Identify the blood parasite species.
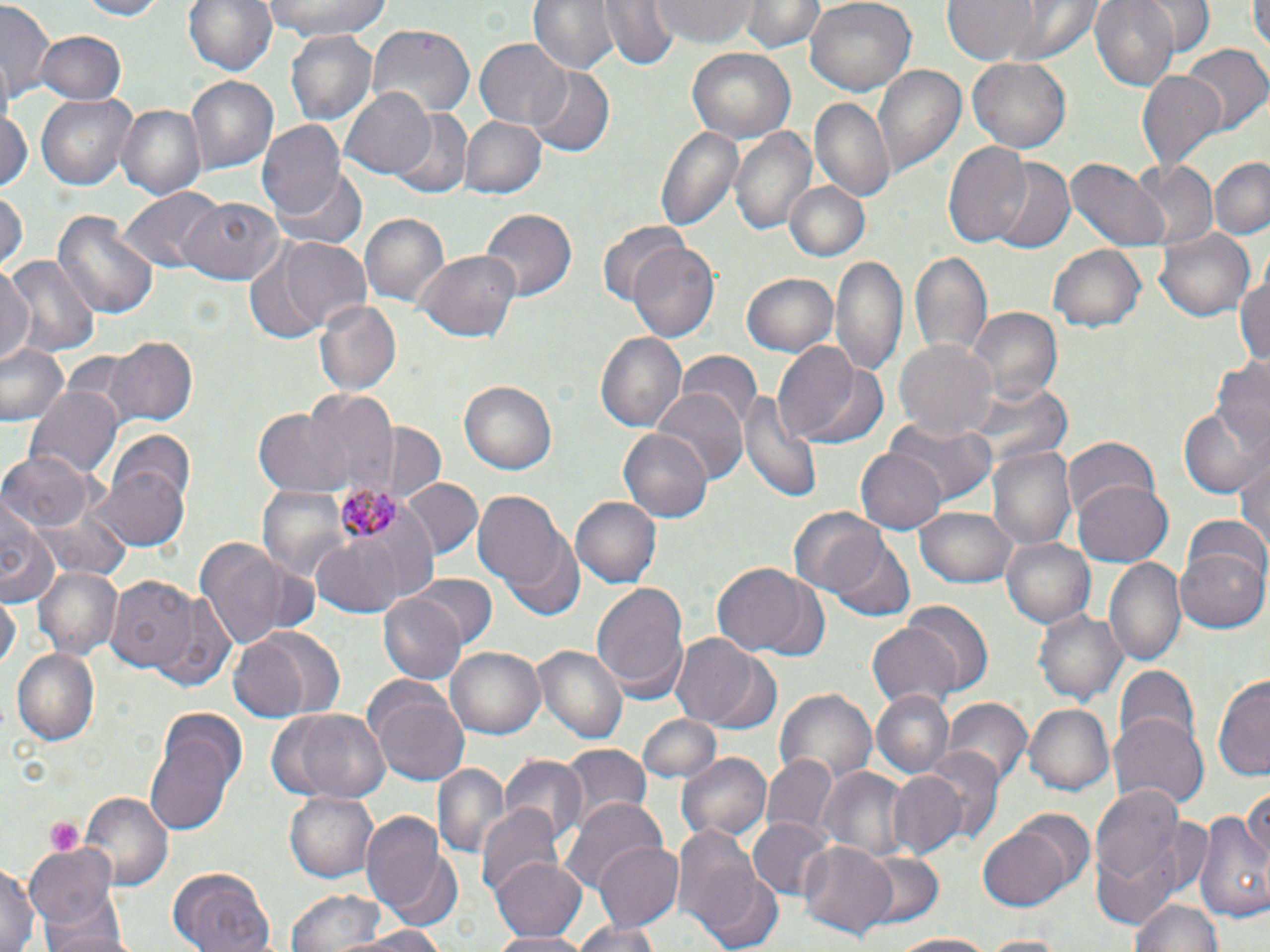

Plasmodium malariae.

stain = May-Grünwald-Giemsa
platelet locations = approximate bounding boxes as [x1, y1, x2, y2] in pixels: [45, 816, 84, 857]
preparation = thin blood smear
magnification = 1000x
uninfected red blood cell locations = approximate bounding boxes as [x1, y1, x2, y2] in pixels: [71, 0, 173, 20], [184, 0, 276, 80], [256, 0, 396, 42], [530, 0, 620, 76], [599, 0, 679, 71], [650, 0, 756, 46], [745, 0, 822, 55], [804, 0, 916, 96], [943, 0, 1041, 68], [1090, 0, 1180, 90], [1144, 0, 1214, 56], [1252, 0, 1270, 57], [0, 3, 56, 107], [366, 26, 475, 122], [37, 31, 126, 105], [286, 33, 382, 130], [476, 38, 573, 130], [1181, 44, 1268, 134], [687, 47, 795, 144], [969, 57, 1071, 155], [873, 64, 965, 176], [529, 68, 615, 155], [1136, 71, 1227, 173], [185, 76, 277, 175], [341, 87, 436, 181], [35, 92, 136, 190], [809, 99, 894, 200], [119, 103, 206, 197], [1, 108, 32, 189], [396, 110, 470, 196], [458, 114, 545, 199], [258, 122, 347, 219], [654, 125, 745, 233], [731, 125, 816, 237], [941, 142, 1036, 247], [1211, 155, 1270, 241], [980, 157, 1076, 252], [1069, 159, 1169, 253], [1125, 159, 1217, 251], [274, 165, 367, 250], [783, 182, 869, 261], [121, 188, 223, 275], [0, 191, 25, 271], [180, 198, 280, 283], [480, 207, 577, 302], [54, 209, 157, 321], [359, 213, 450, 313], [595, 222, 691, 310], [1155, 227, 1254, 322], [247, 234, 369, 342], [627, 242, 720, 345], [1050, 244, 1146, 332], [416, 250, 520, 342], [910, 251, 991, 359], [4, 252, 100, 357], [833, 253, 908, 378], [0, 262, 32, 366], [1234, 263, 1270, 371], [742, 271, 838, 356], [314, 299, 401, 395], [964, 306, 1063, 408], [595, 332, 686, 434], [104, 335, 197, 427], [894, 339, 997, 443], [774, 340, 864, 445], [3, 342, 68, 426], [676, 353, 763, 432], [1209, 357, 1270, 453], [460, 382, 558, 474], [958, 383, 1070, 468], [25, 385, 122, 485], [656, 386, 747, 483], [740, 389, 821, 506], [306, 391, 398, 495], [1178, 405, 1267, 498], [255, 407, 352, 496], [887, 416, 997, 503], [376, 422, 443, 500], [616, 428, 713, 523], [106, 431, 196, 515], [1063, 439, 1161, 524], [1235, 444, 1270, 560], [989, 446, 1077, 549], [855, 448, 945, 534], [0, 450, 92, 534], [96, 467, 189, 551], [400, 478, 483, 560], [1074, 478, 1172, 566], [258, 482, 353, 581], [472, 491, 568, 593], [0, 496, 58, 606], [571, 497, 660, 588], [324, 499, 440, 606], [788, 506, 888, 597], [915, 506, 1018, 587], [1182, 512, 1270, 595], [501, 534, 586, 619], [195, 536, 301, 646], [827, 537, 915, 619], [1001, 537, 1099, 627], [316, 539, 401, 617], [1175, 543, 1270, 634], [1106, 556, 1185, 665], [712, 560, 814, 658], [34, 565, 122, 658], [409, 575, 497, 649], [104, 576, 198, 673], [590, 578, 690, 702], [152, 594, 239, 691], [0, 595, 19, 674], [377, 595, 465, 687], [900, 601, 995, 695], [1036, 607, 1126, 705], [867, 619, 962, 709], [227, 630, 333, 721], [677, 634, 777, 732], [535, 644, 626, 744], [449, 646, 544, 740], [11, 647, 101, 745], [1114, 665, 1199, 754], [1213, 673, 1270, 779], [367, 683, 469, 786], [773, 686, 878, 784], [870, 690, 954, 778], [944, 699, 1032, 787], [1025, 703, 1113, 796], [268, 708, 390, 802], [638, 714, 721, 785], [1110, 717, 1208, 809], [144, 728, 238, 835], [560, 744, 650, 831], [918, 748, 1005, 844], [677, 752, 771, 843], [761, 754, 838, 839], [500, 755, 587, 852], [817, 763, 911, 862], [436, 765, 508, 857], [884, 769, 968, 860], [1244, 780, 1270, 872], [1088, 781, 1186, 916], [81, 790, 174, 887], [286, 790, 379, 882], [560, 798, 668, 904], [477, 804, 563, 904], [1197, 806, 1270, 925], [362, 810, 451, 923], [746, 815, 834, 900], [673, 821, 768, 942], [976, 824, 1075, 912], [592, 842, 683, 932], [798, 843, 896, 938], [25, 844, 120, 932], [857, 852, 944, 927], [492, 857, 590, 940], [0, 859, 41, 952], [167, 869, 275, 952], [696, 870, 784, 952], [284, 888, 393, 952], [1132, 899, 1225, 952], [42, 903, 129, 952], [572, 920, 665, 952], [333, 928, 454, 951], [485, 931, 596, 952], [888, 931, 1003, 950], [975, 936, 1072, 952]
modality = optical microscopy
image size = 1270×952 pixels
Plasmodium malariae-infected red blood cell locations = approximate bounding boxes as [x1, y1, x2, y2] in pixels: [334, 475, 408, 547]
field of view = single